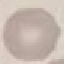

malaria_status: uninfected
stain: Giemsa
preparation: thin smear
image_type: cell patch, automatically extracted from a larger field of view and resized to 64 × 64 pixels
capture: smartphone through the microscope eyepiece